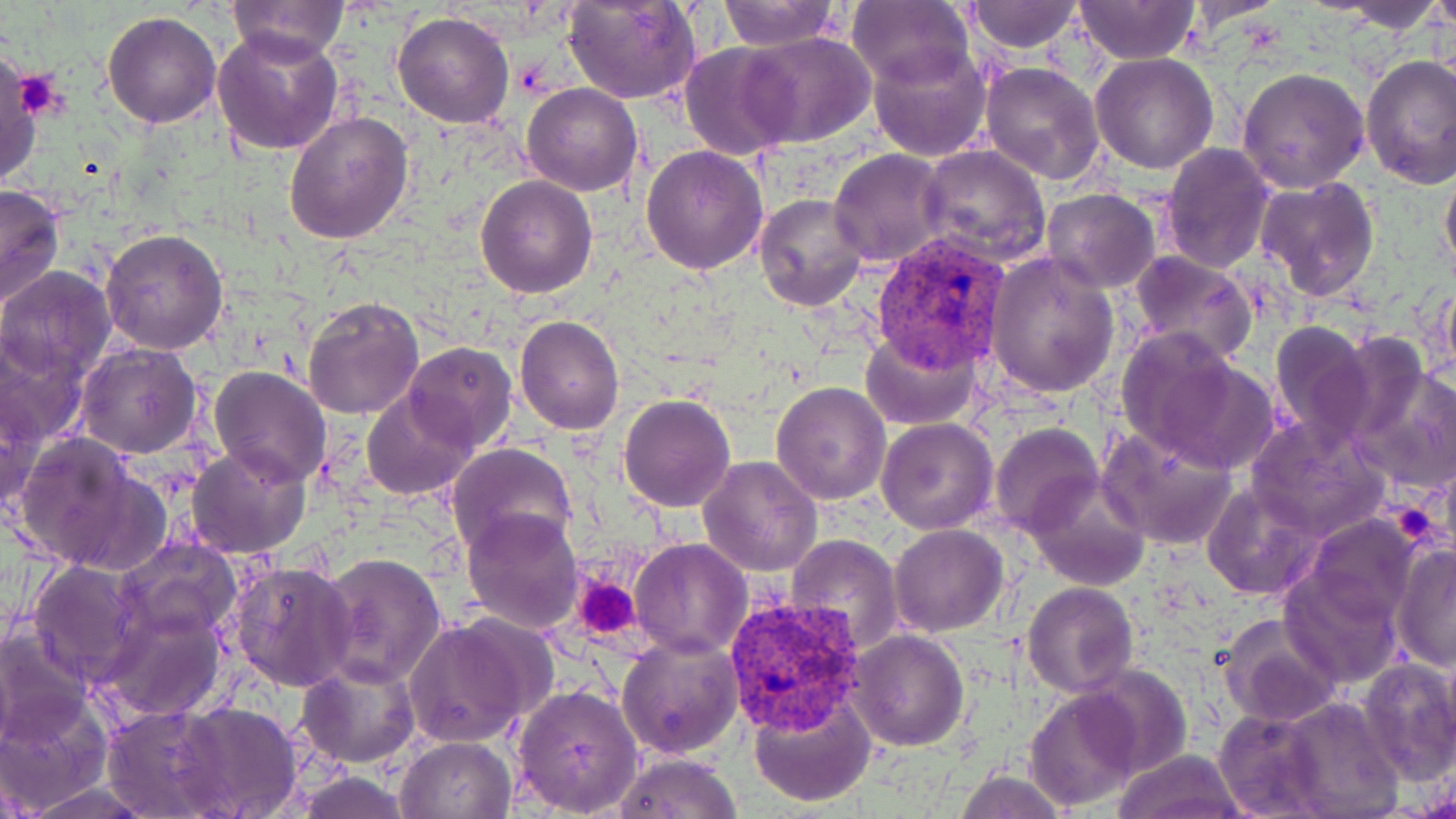 Approximate bounding boxes as (x1, y1, x2, y2) in pixels. Platelet locations: (17, 71, 70, 120), (1388, 504, 1440, 549), (573, 575, 641, 638). Plasmodium vivax-infected red blood cell locations: (871, 233, 1011, 375), (724, 593, 867, 736). Uninfected red blood cell locations: (227, 0, 347, 62), (716, 0, 842, 50), (1334, 0, 1450, 32), (1425, 0, 1454, 33), (563, 1, 699, 104), (846, 1, 973, 86), (965, 1, 1085, 52), (1073, 1, 1200, 66), (102, 10, 223, 130), (392, 10, 516, 129), (214, 30, 344, 156), (742, 32, 875, 148), (679, 43, 798, 159), (869, 44, 995, 163), (1091, 52, 1219, 174), (0, 53, 41, 192), (1361, 56, 1456, 190), (980, 63, 1104, 185), (1235, 67, 1370, 192), (522, 83, 642, 196), (284, 110, 415, 245), (1160, 143, 1277, 273), (640, 144, 767, 277), (919, 144, 1051, 267), (829, 148, 952, 268), (1440, 157, 1456, 285), (475, 176, 597, 298), (1255, 177, 1380, 301), (0, 184, 66, 312), (1042, 189, 1160, 292), (753, 193, 869, 310), (101, 227, 231, 355), (1127, 249, 1257, 366), (985, 253, 1119, 398), (0, 266, 117, 384), (1430, 280, 1456, 389), (302, 296, 424, 421), (514, 315, 625, 436), (1268, 321, 1372, 453), (1114, 327, 1252, 464), (861, 328, 981, 430), (1327, 329, 1430, 451), (0, 331, 87, 453), (404, 342, 517, 453), (76, 343, 202, 459), (1352, 357, 1456, 492), (209, 366, 332, 486), (770, 380, 891, 504), (1, 384, 45, 517), (361, 388, 478, 500), (618, 393, 737, 511), (876, 417, 997, 534), (1248, 419, 1389, 539), (989, 422, 1103, 537), (1098, 426, 1240, 550), (13, 434, 163, 574), (447, 442, 578, 558), (187, 444, 311, 557), (697, 455, 822, 575), (1024, 473, 1151, 592), (1201, 481, 1319, 599), (460, 505, 583, 633), (1304, 513, 1421, 628), (889, 525, 1010, 638), (785, 535, 904, 655), (116, 537, 242, 644), (629, 538, 751, 660), (1390, 543, 1456, 672), (317, 552, 447, 690), (228, 558, 357, 691), (27, 559, 144, 683), (1278, 567, 1403, 688), (1022, 582, 1139, 696), (100, 606, 227, 722), (1217, 613, 1345, 729), (402, 615, 549, 748), (0, 627, 93, 747), (850, 629, 967, 751), (617, 636, 742, 757), (1356, 655, 1456, 785), (298, 658, 420, 769), (1073, 663, 1192, 780), (511, 682, 644, 817), (1024, 686, 1143, 811), (747, 692, 876, 807), (0, 696, 108, 812), (1275, 696, 1405, 817), (168, 701, 306, 818), (101, 705, 233, 817), (1212, 709, 1327, 817), (396, 736, 517, 819), (1113, 748, 1247, 819), (612, 750, 743, 818), (951, 770, 1073, 819), (294, 771, 412, 819), (18, 780, 158, 818). Slide-level diagnosis: Plasmodium vivax. Thin blood smear. Image is 1456×819 pixels. Optical microscopy. Single field of view. 1000x magnification. May-Grünwald-Giemsa stain.